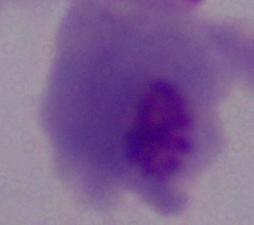
1000x magnification. Photomicrograph. A trichomonad is shown.